Assess for malaria.
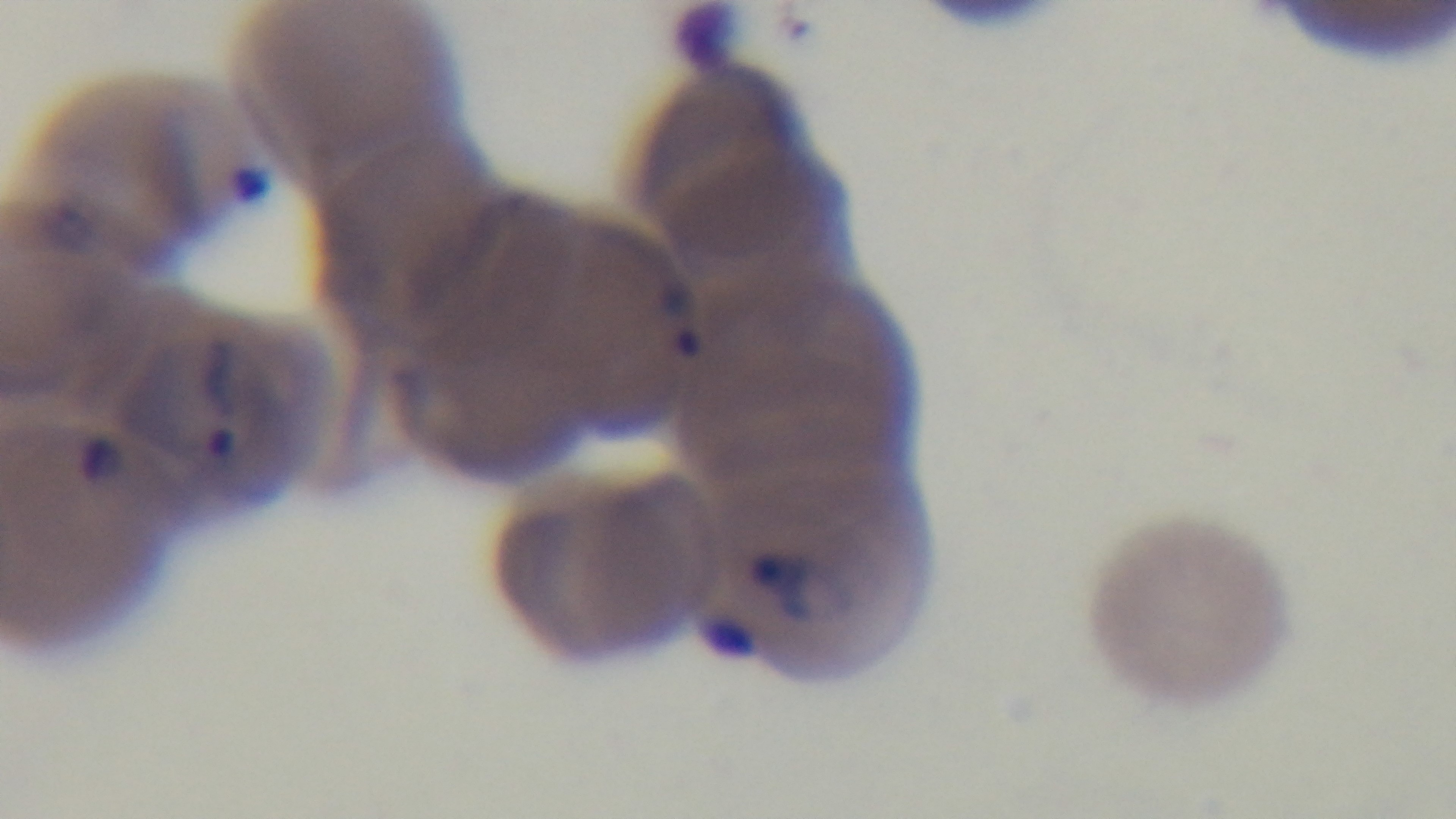
It is infected.

modality = light microscopy
stain = Giemsa
capture = mounted 4K digital camera
objective = 100x oil immersion
field of view = one from the slide
preparation = thin